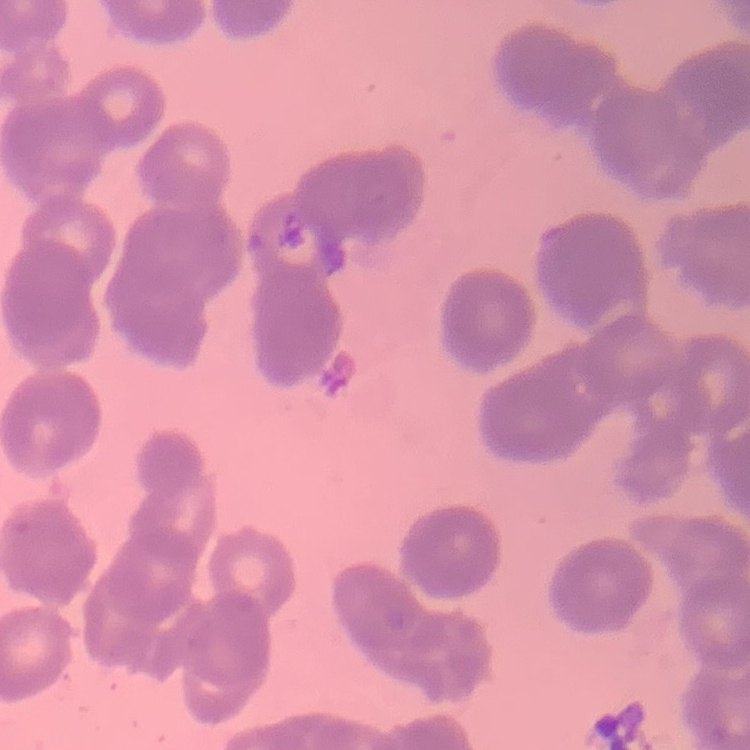 The red blood cells show rouleaux formation. Thin blood smear. Stained with either Field's or Giemsa. One tile cut from a larger photomicrograph.